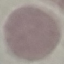
result: negative for malaria parasites
capture: smartphone camera at the microscope eyepiece
preparation: thin blood smear
image_type: automatically extracted cell patch, resized to 64 × 64 pixels
stain: Giemsa